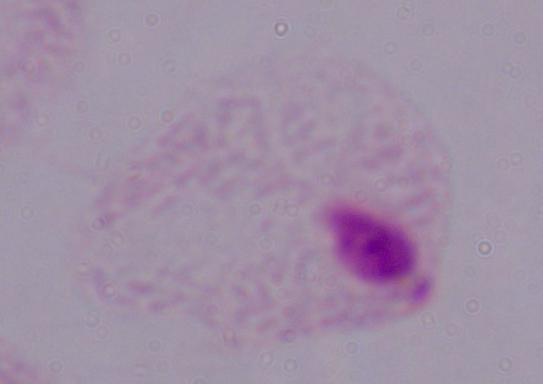 A trichomonad is shown. Micrograph. 1000x magnification.